State the preparation type.
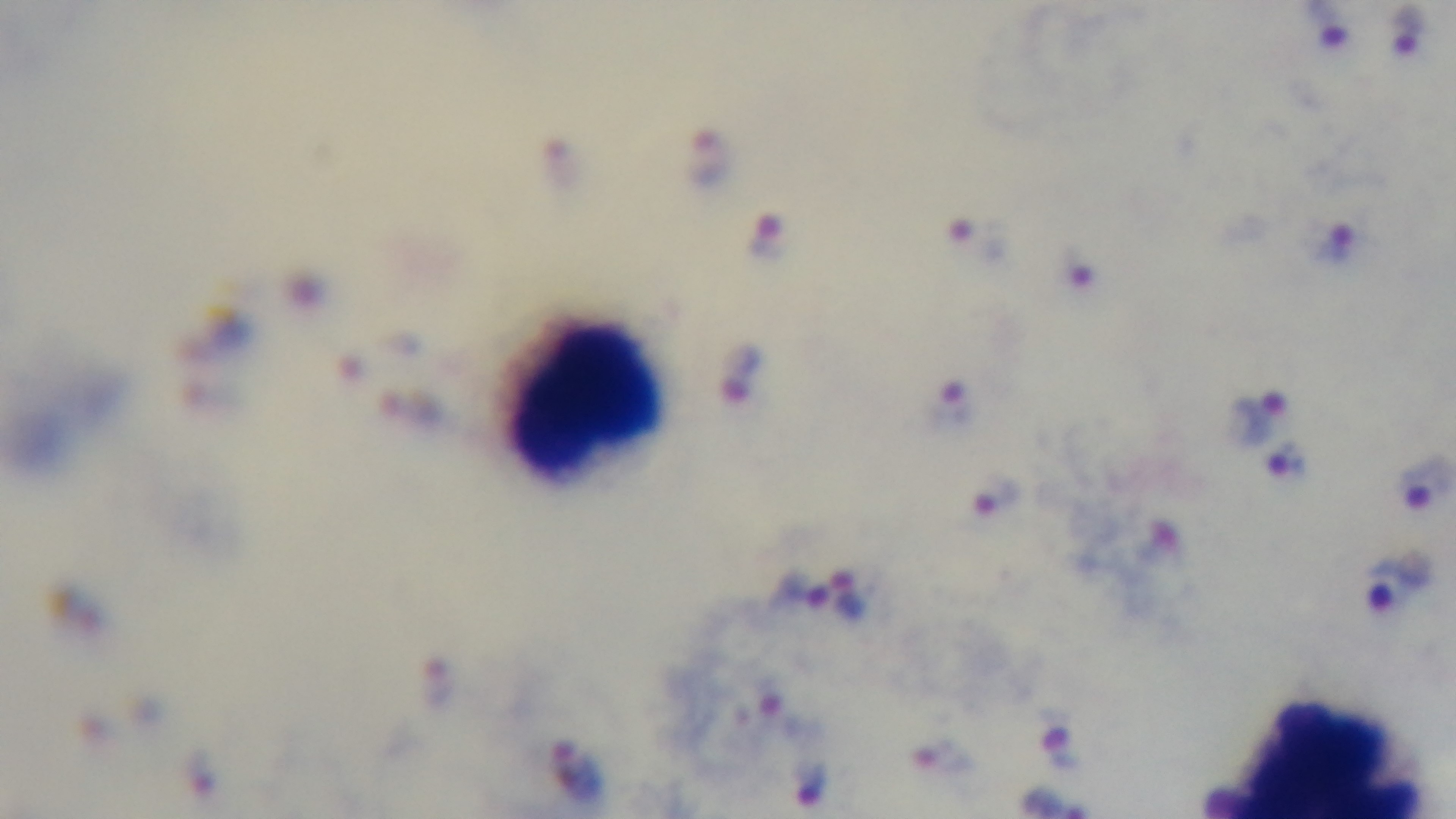

Thick.

malaria status = infected
capture = mounted 4K digital camera
objective = 100x oil immersion
field of view = one from the slide
modality = light microscopy
stain = Giemsa